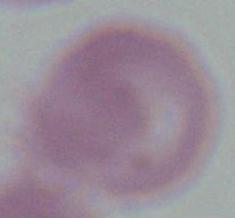

Summary:
  - Magnification: 1000x
  - Identification: erythrocyte
  - Modality: photomicrograph